Classify this cell by malaria status.
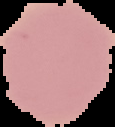
It is uninfected.

image type = cell region segmented out of the field of view; surrounding area masked to black
preparation = thin blood smear
image size = 115×127 pixels